Assess this cell for malaria.
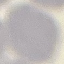
Uninfected.

Acquired by smartphone through the microscope eyepiece. Cell patch, automatically extracted from a larger field of view and resized to 64 × 64 pixels. Giemsa-stained preparation. Thin blood film.